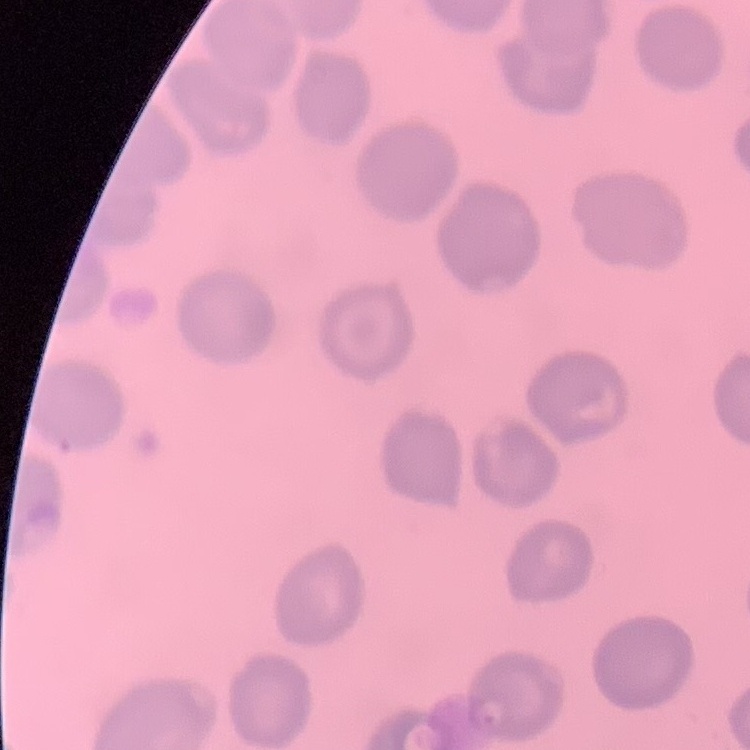
The red blood cells exhibit no rouleaux formation. Thin peripheral smear. One tile cut from a larger photomicrograph. Field's or Giemsa stain.